Identify the parasite.
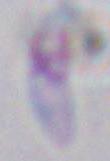

Toxoplasma gondii.

1000x magnification. Micrograph.